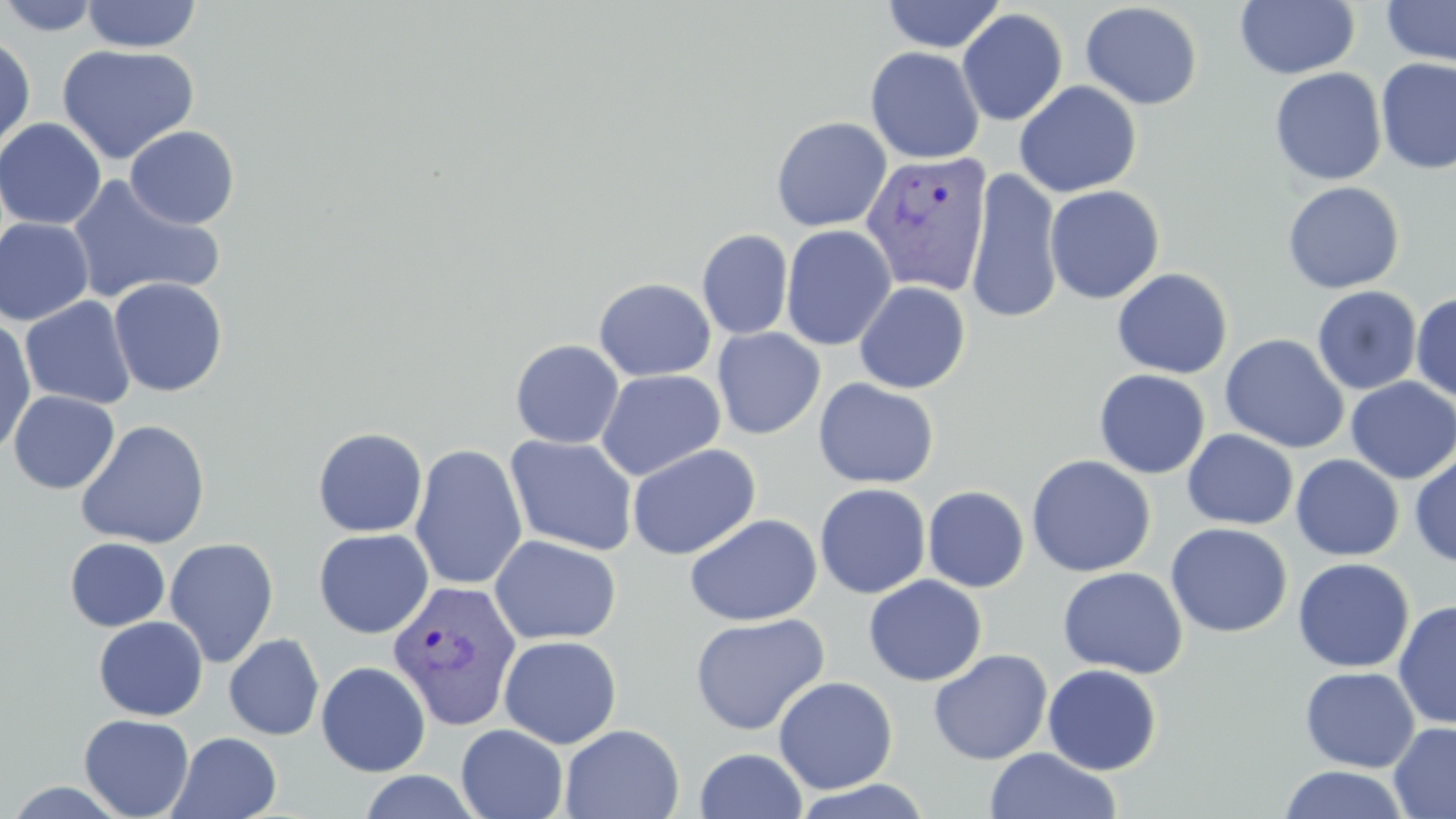
Summary:
  - Coordinate format: approximate bounding boxes as (x1,y1)-(x2,y2) corner pairs in pixels
  - Plasmodium vivax-infected red blood cell locations: (860,150)-(993,297), (387,579)-(521,731)
  - Uninfected red blood cell locations: (1,0)-(102,36), (81,0)-(201,53), (880,0)-(1006,53), (1234,0)-(1360,80), (1381,1)-(1456,68), (1080,2)-(1203,110), (957,8)-(1069,126), (0,35)-(36,156), (57,44)-(200,164), (865,46)-(985,164), (1375,57)-(1456,174), (1269,67)-(1387,186), (1014,81)-(1141,197), (771,116)-(892,231), (0,117)-(107,231), (124,125)-(240,229), (965,169)-(1064,324), (66,175)-(225,305), (1282,181)-(1405,294), (1045,185)-(1165,305), (0,217)-(95,326), (780,225)-(897,351), (697,229)-(794,340), (1111,267)-(1233,379), (108,277)-(228,397), (594,277)-(716,381), (853,281)-(971,394), (1312,285)-(1422,395), (1411,291)-(1456,402), (20,296)-(136,410), (0,318)-(36,455), (712,327)-(825,439), (1220,333)-(1350,454), (510,339)-(625,449), (596,369)-(725,480), (1093,369)-(1210,479), (1345,377)-(1456,483), (813,378)-(939,489), (9,390)-(119,494), (75,419)-(211,549), (313,427)-(428,537), (1182,429)-(1299,530), (505,434)-(639,556), (627,443)-(761,560), (409,444)-(527,590), (1409,452)-(1456,567), (1291,454)-(1404,561), (1026,455)-(1156,577), (814,483)-(931,598), (922,486)-(1030,592), (684,513)-(822,627), (1165,522)-(1292,638), (313,528)-(434,638), (489,535)-(621,645), (65,537)-(170,631), (165,537)-(280,668), (1292,558)-(1414,673), (1057,566)-(1189,679), (863,575)-(987,686), (1393,600)-(1456,728), (689,613)-(830,736), (93,616)-(208,721), (224,634)-(325,740), (498,635)-(622,749), (928,649)-(1053,765), (316,661)-(431,776), (1043,663)-(1162,775), (1300,667)-(1420,771), (774,676)-(898,794), (78,714)-(194,819), (1389,721)-(1456,818), (456,724)-(568,819), (559,724)-(685,819), (168,732)-(282,819), (984,747)-(1121,819), (694,748)-(808,819), (1278,765)-(1409,819), (357,770)-(482,818), (789,779)-(936,819), (1,781)-(133,818)
  - Slide-level diagnosis: Plasmodium vivax
  - Field of view: single
  - Stain: May-Grünwald-Giemsa
  - Image size: 1456×819 pixels
  - Preparation: thin blood smear
  - Magnification: 1000x
  - Modality: optical microscopy